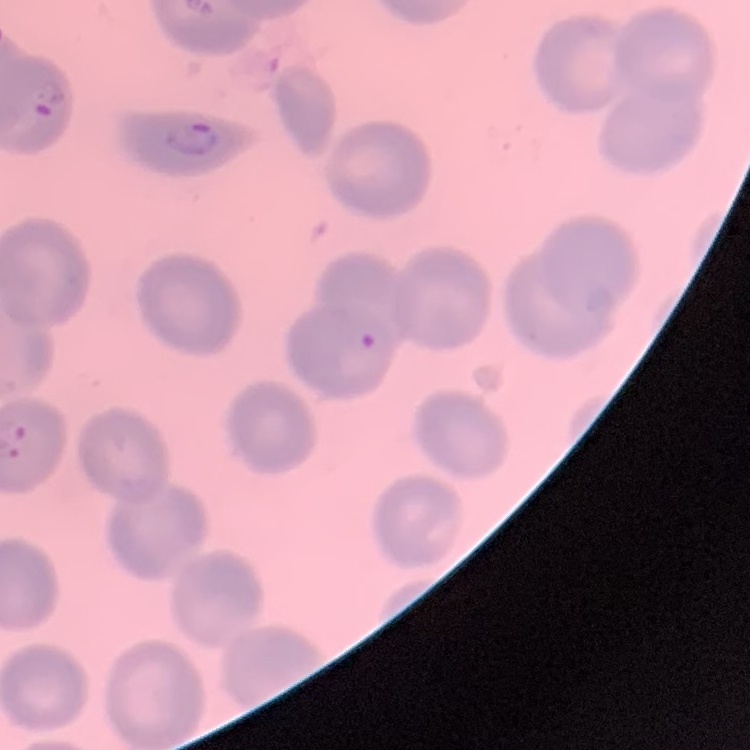

The red blood cells show no rouleaux formation. Thin peripheral smear. One tile cut from a larger photomicrograph. Field's or Giemsa stain.